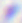

Summary:
  - Identification: Toxoplasma gondii
  - Modality: micrograph
  - Magnification: 400x